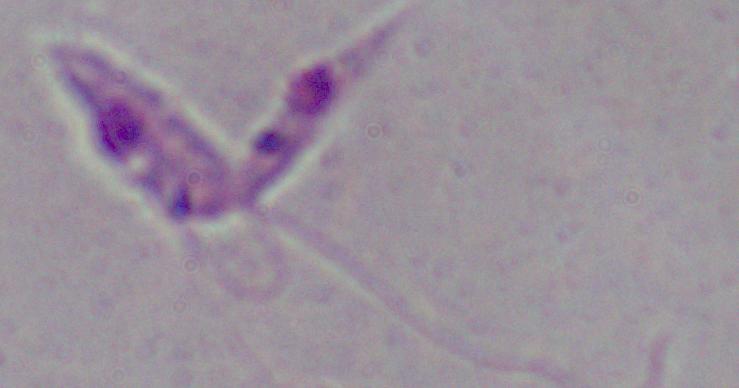

1000x magnification. Micrograph. A Leishmania parasite is shown.